Report the malaria status of this cell.
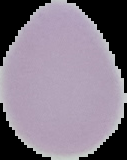
Uninfected.

Summary:
  - Image size: 127×160 pixels
  - Image type: cell region segmented out of the field of view; surrounding area masked to black
  - Preparation: thin blood film